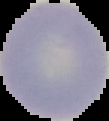

{
  "preparation": "thin blood smear",
  "malaria_status": "uninfected",
  "image_size": "109×121 pixels",
  "image_type": "segmented cell region with the area outside set to black"
}